Classify this cell by malaria status.
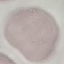
It is uninfected.

Summary:
  - Capture: smartphone through the microscope eyepiece
  - Stain: Giemsa
  - Image type: cell patch, automatically extracted from a larger field of view and resized to 64 × 64 pixels
  - Preparation: thin blood smear